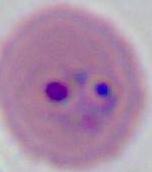 Captured at either 400x or 1000x magnification. A Plasmodium parasite is shown. Micrograph.